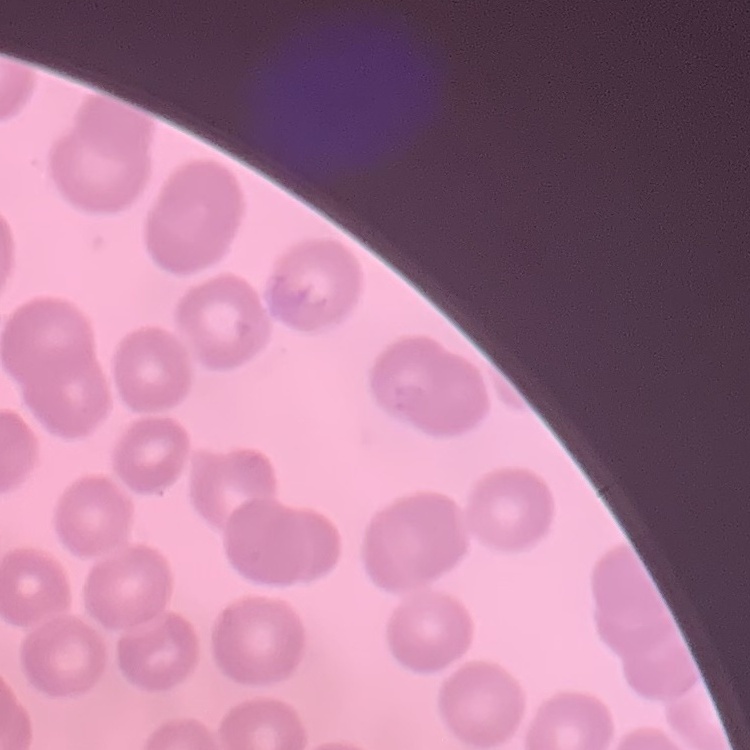 The erythrocytes show no rouleaux formation. One tile cut from a larger photomicrograph. Thin blood film. Field's or Giemsa stain.